Locate every blood parasite and identify its species.
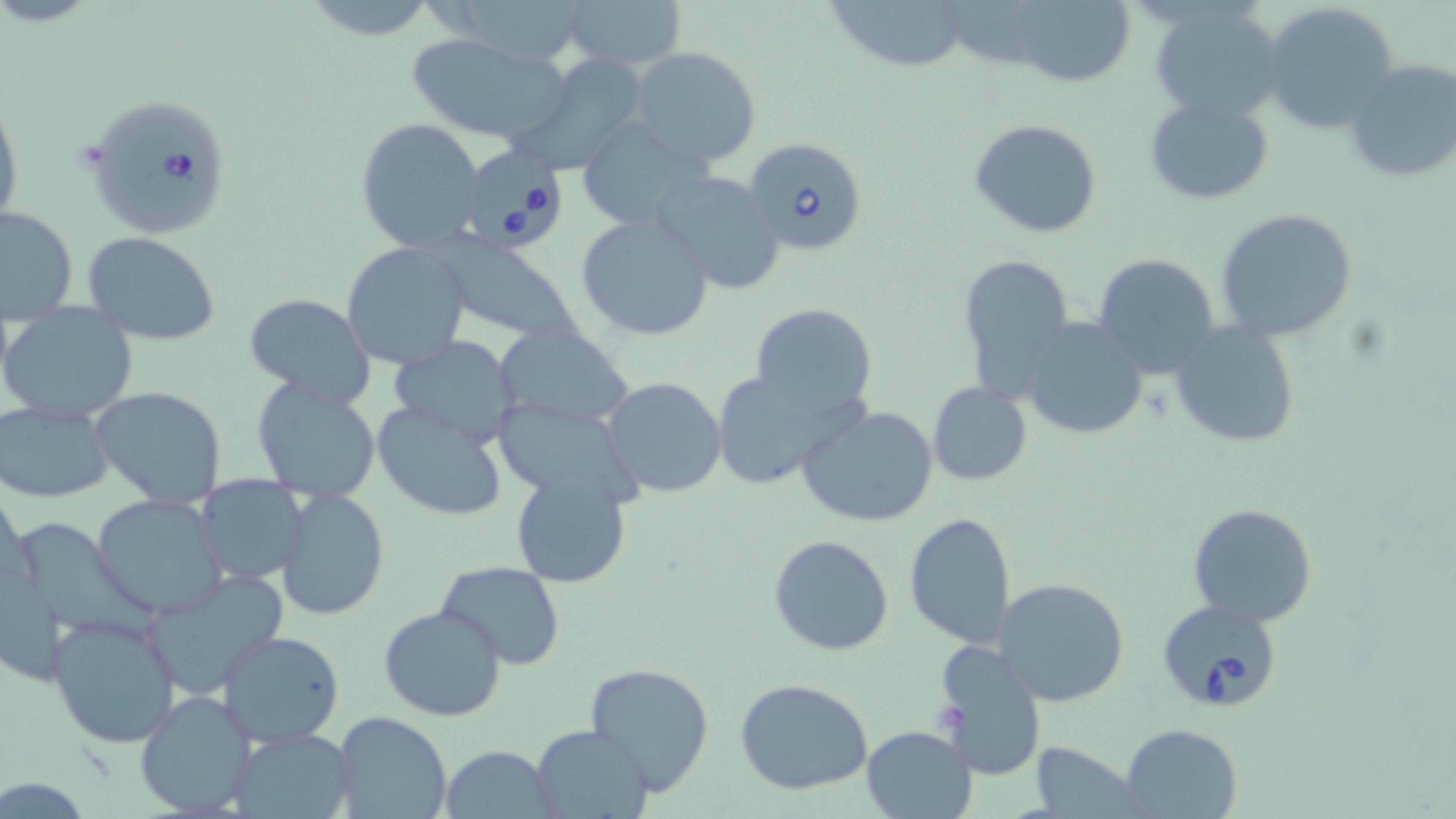

Approximate bounding boxes as [x1, y1, x2, y2] in pixels.
Babesia divergens-infected red blood cells: [86, 100, 233, 232], [744, 138, 870, 257], [467, 142, 568, 255], [1158, 599, 1284, 712].
No Plasmodium falciparum, Plasmodium ovale, Plasmodium malariae, Plasmodium vivax, or Trypanosoma brucei observed.

slide-level diagnosis = Babesia divergens
field of view = one of a larger specimen
preparation = thin blood smear
modality = light microscopy
image size = 1456×819 pixels
uninfected red blood cell locations = approximate bounding boxes as [x1, y1, x2, y2] in pixels: [560, 0, 686, 73], [826, 0, 973, 74], [1004, 1, 1139, 89], [1262, 2, 1398, 132], [1150, 3, 1287, 122], [404, 31, 571, 146], [627, 47, 764, 168], [1341, 57, 1456, 183], [519, 60, 647, 172], [0, 94, 23, 231], [1143, 94, 1276, 205], [356, 118, 487, 255], [970, 119, 1101, 238], [586, 129, 725, 221], [651, 169, 787, 294], [0, 206, 78, 320], [1214, 207, 1358, 342], [575, 212, 714, 341], [83, 232, 221, 344], [432, 234, 584, 349], [341, 241, 470, 371], [955, 252, 1075, 400], [1090, 253, 1218, 376], [244, 294, 374, 409], [750, 304, 878, 419], [4, 306, 138, 423], [1018, 318, 1150, 442], [1169, 321, 1300, 449], [494, 324, 634, 431], [392, 333, 520, 440], [707, 369, 853, 491], [251, 377, 381, 506], [602, 377, 726, 497], [927, 382, 1032, 485], [88, 386, 228, 510], [371, 399, 510, 523], [1, 402, 114, 504], [795, 405, 940, 529], [510, 470, 632, 589], [195, 475, 307, 586], [278, 486, 388, 621], [92, 492, 227, 618], [1187, 502, 1317, 628], [903, 511, 1016, 653], [22, 521, 163, 637], [769, 536, 894, 657], [435, 560, 565, 671], [143, 570, 290, 700], [996, 576, 1131, 707], [377, 603, 508, 722], [47, 609, 182, 749], [218, 630, 345, 747], [934, 640, 1046, 780], [583, 662, 715, 795], [735, 679, 876, 795], [133, 690, 258, 818], [333, 711, 452, 819], [860, 724, 979, 819], [1120, 724, 1242, 817], [529, 725, 653, 817], [226, 728, 354, 818], [1025, 741, 1147, 817], [441, 743, 557, 817]
magnification = 1000x
stain = May-Grünwald-Giemsa